Report the malaria status of this cell.
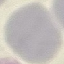

Uninfected.

Automatically extracted cell patch, resized to 64 × 64 pixels. Acquired by smartphone through the microscope eyepiece. Thin blood film. Giemsa stain.